Point out each malaria parasite and each leukocyte.
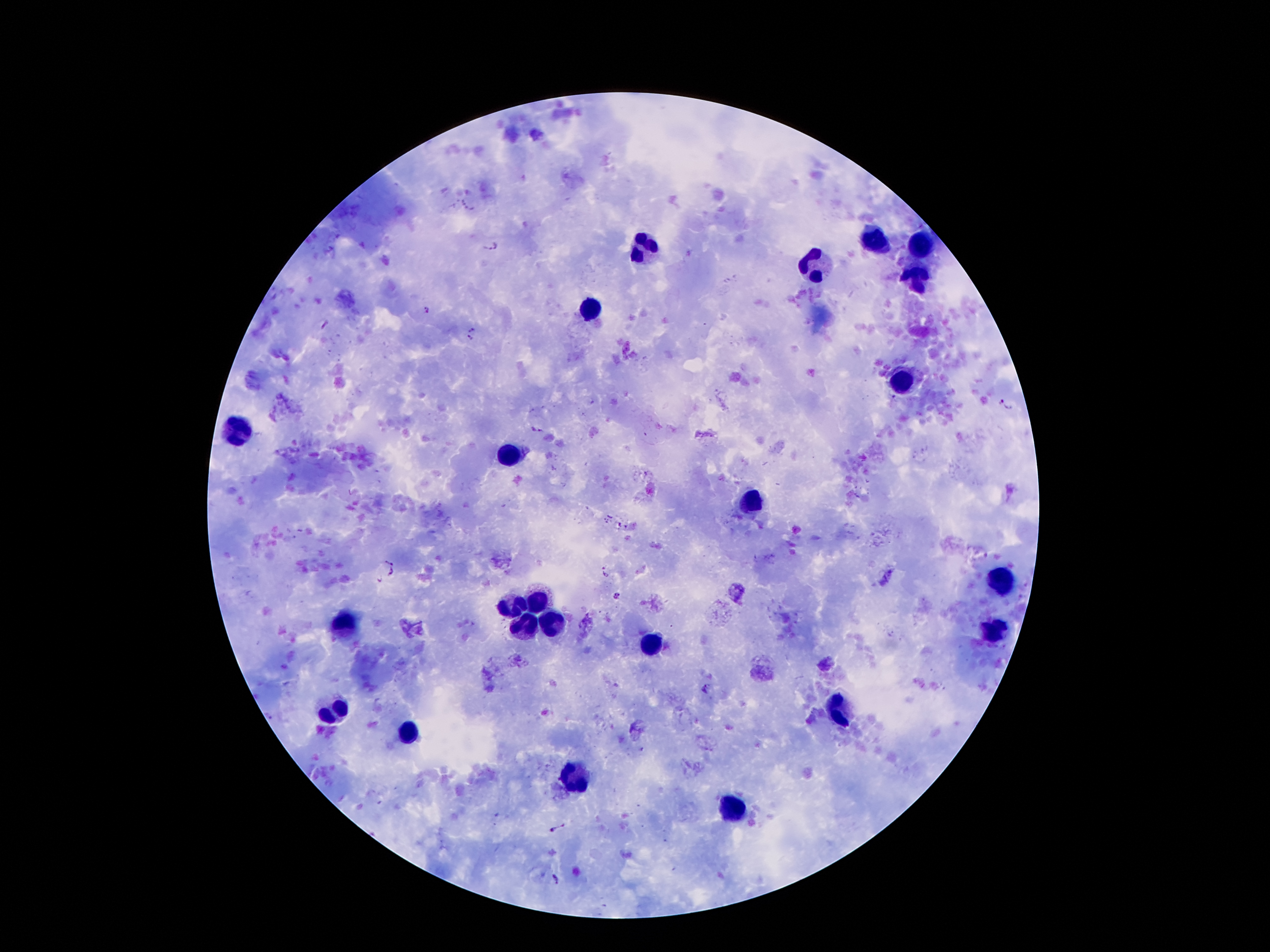

Approximate object centers, in pixels from the top-left corner.
Malaria parasites: (x=493, y=247), (x=426, y=312), (x=322, y=324), (x=472, y=328), (x=469, y=340), (x=1000, y=402), (x=1007, y=408), (x=536, y=430), (x=391, y=560), (x=606, y=571), (x=391, y=572), (x=378, y=578), (x=616, y=596), (x=707, y=688), (x=557, y=829), (x=557, y=877).
Leukocytes: (x=645, y=245), (x=921, y=245), (x=876, y=247), (x=813, y=266), (x=918, y=275), (x=591, y=310), (x=902, y=384), (x=236, y=432), (x=513, y=457), (x=753, y=501), (x=998, y=581), (x=540, y=598), (x=515, y=611), (x=553, y=621), (x=343, y=623), (x=528, y=630), (x=992, y=632), (x=650, y=649), (x=839, y=710), (x=337, y=712), (x=406, y=731), (x=574, y=771), (x=730, y=804).

{
  "patient_malaria_status": "infected with Plasmodium falciparum",
  "magnification": "100x",
  "image_size": "1270×952 pixels",
  "field_of_view": "single",
  "capture": "smartphone through the microscope eyepiece",
  "stain": "Giemsa",
  "preparation": "thick blood film"
}